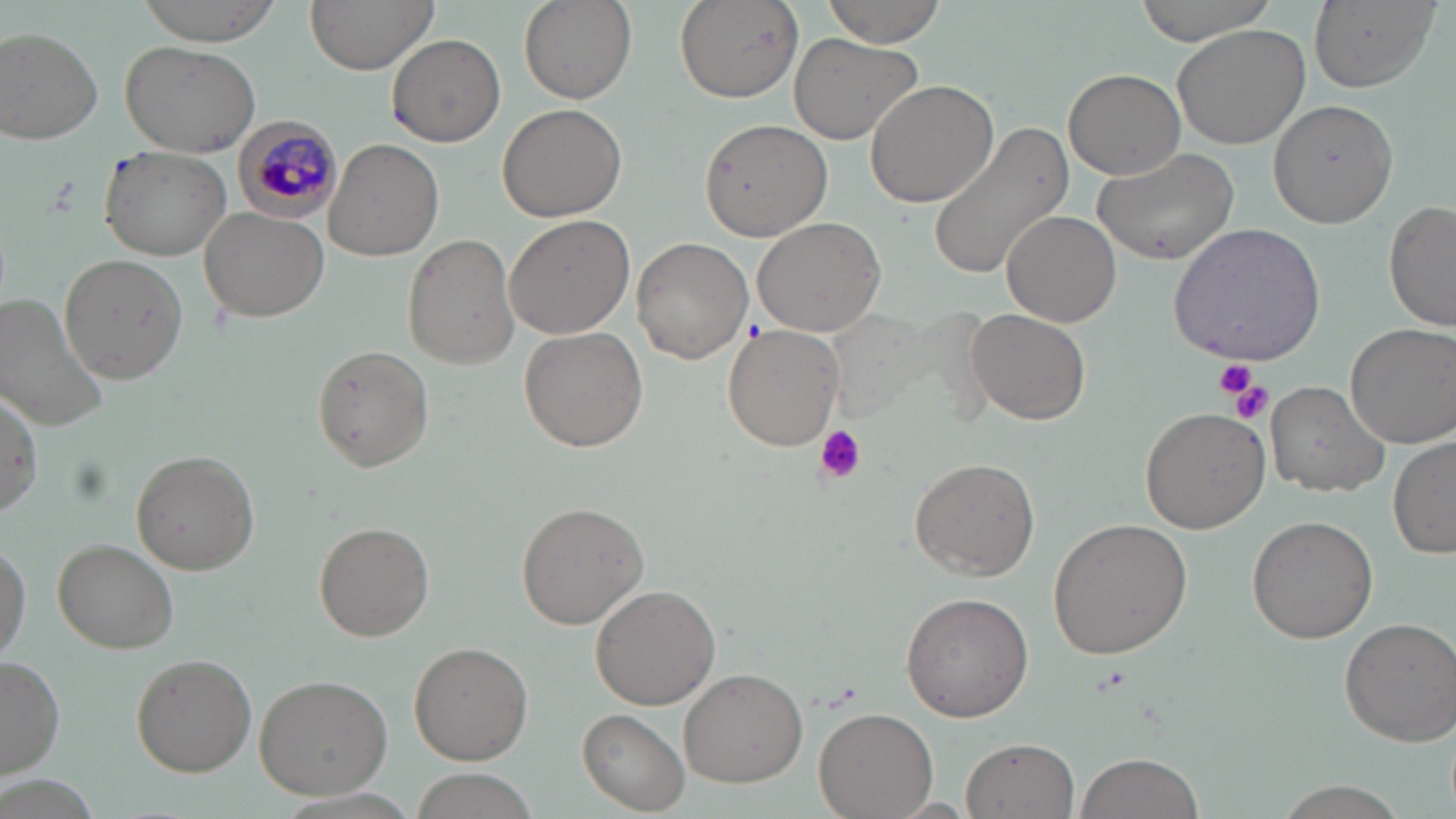
{
  "plasmodium_malariae_infected_red_blood_cell_locations": "approximate bounding boxes as [x1, y1, x2, y2] in pixels: [232, 117, 342, 216]",
  "slide_level_diagnosis": "Plasmodium malariae",
  "magnification": "1000x",
  "preparation": "thin blood film",
  "modality": "light microscopy",
  "image_size": "1456×819 pixels",
  "field_of_view": "one of a larger specimen",
  "platelet_locations": "approximate bounding boxes as [x1, y1, x2, y2] in pixels: [1213, 356, 1257, 397], [1227, 379, 1271, 427], [814, 425, 865, 481]",
  "stain": "May-Grünwald-Giemsa",
  "uninfected_red_blood_cell_locations": "approximate bounding boxes as [x1, y1, x2, y2] in pixels: [135, 0, 283, 43], [305, 0, 438, 73], [520, 0, 636, 104], [674, 0, 803, 102], [821, 0, 948, 45], [1133, 0, 1282, 44], [1308, 1, 1440, 92], [1173, 22, 1313, 149], [2, 28, 103, 144], [788, 33, 925, 146], [387, 34, 506, 147], [120, 39, 262, 157], [1063, 68, 1187, 180], [865, 80, 999, 209], [1269, 98, 1397, 227], [497, 104, 626, 222], [700, 119, 833, 241], [927, 121, 1074, 281], [324, 138, 444, 262], [97, 145, 232, 261], [1090, 147, 1240, 264], [1384, 200, 1456, 332], [199, 206, 331, 322], [1003, 211, 1122, 327], [504, 213, 635, 339], [752, 216, 886, 337], [1166, 222, 1326, 364], [402, 234, 521, 369], [631, 237, 752, 364], [58, 253, 187, 386], [0, 291, 110, 430], [965, 307, 1092, 425], [721, 322, 846, 450], [1344, 322, 1456, 447], [518, 325, 649, 451], [310, 345, 435, 471], [1266, 380, 1391, 498], [2, 383, 44, 524], [1140, 406, 1269, 534], [1388, 433, 1455, 560], [128, 449, 260, 575], [909, 456, 1041, 580], [514, 502, 648, 629], [1247, 516, 1377, 645], [1047, 517, 1193, 659], [312, 520, 435, 641], [0, 537, 31, 663], [52, 538, 179, 653], [589, 583, 721, 710], [901, 590, 1036, 722], [1338, 616, 1456, 747], [409, 640, 533, 766], [128, 652, 256, 776], [1, 655, 65, 781], [679, 668, 806, 787], [253, 673, 392, 800], [815, 706, 937, 818], [577, 708, 691, 812], [960, 737, 1080, 818], [1073, 751, 1205, 819], [403, 769, 540, 819], [1268, 784, 1406, 819]"
}